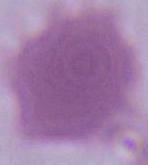 A red blood cell is seen. 1000x magnification. Photomicrograph.